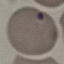

Malaria status: uninfected. Automatically extracted cell patch, resized to 64 × 64 pixels. Thin blood film. Giemsa-stained preparation. Photographed with a smartphone camera at the microscope eyepiece.